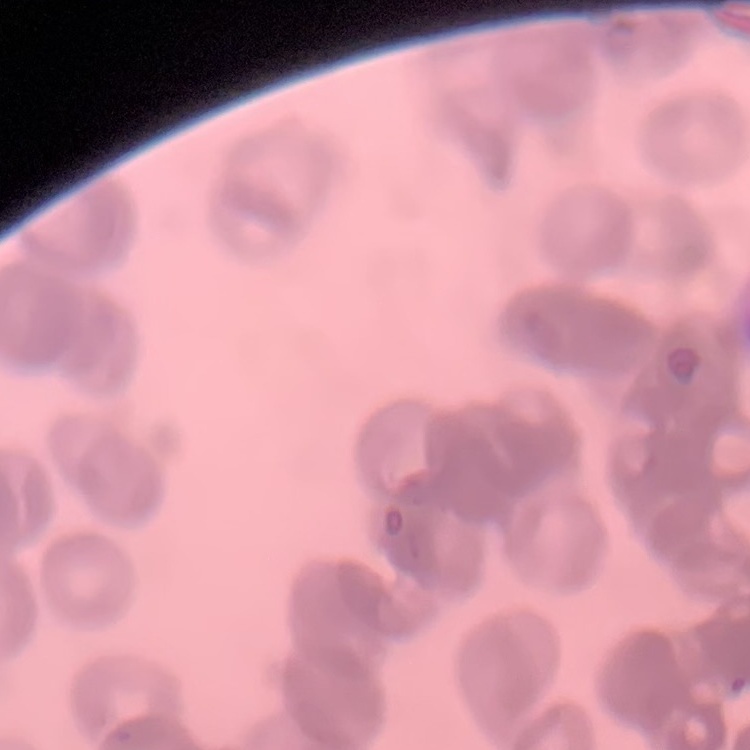

red blood cell morphology = rouleaux formation
stain = Field's or Giemsa
preparation = thin blood film
image type = square crop of a larger photomicrograph